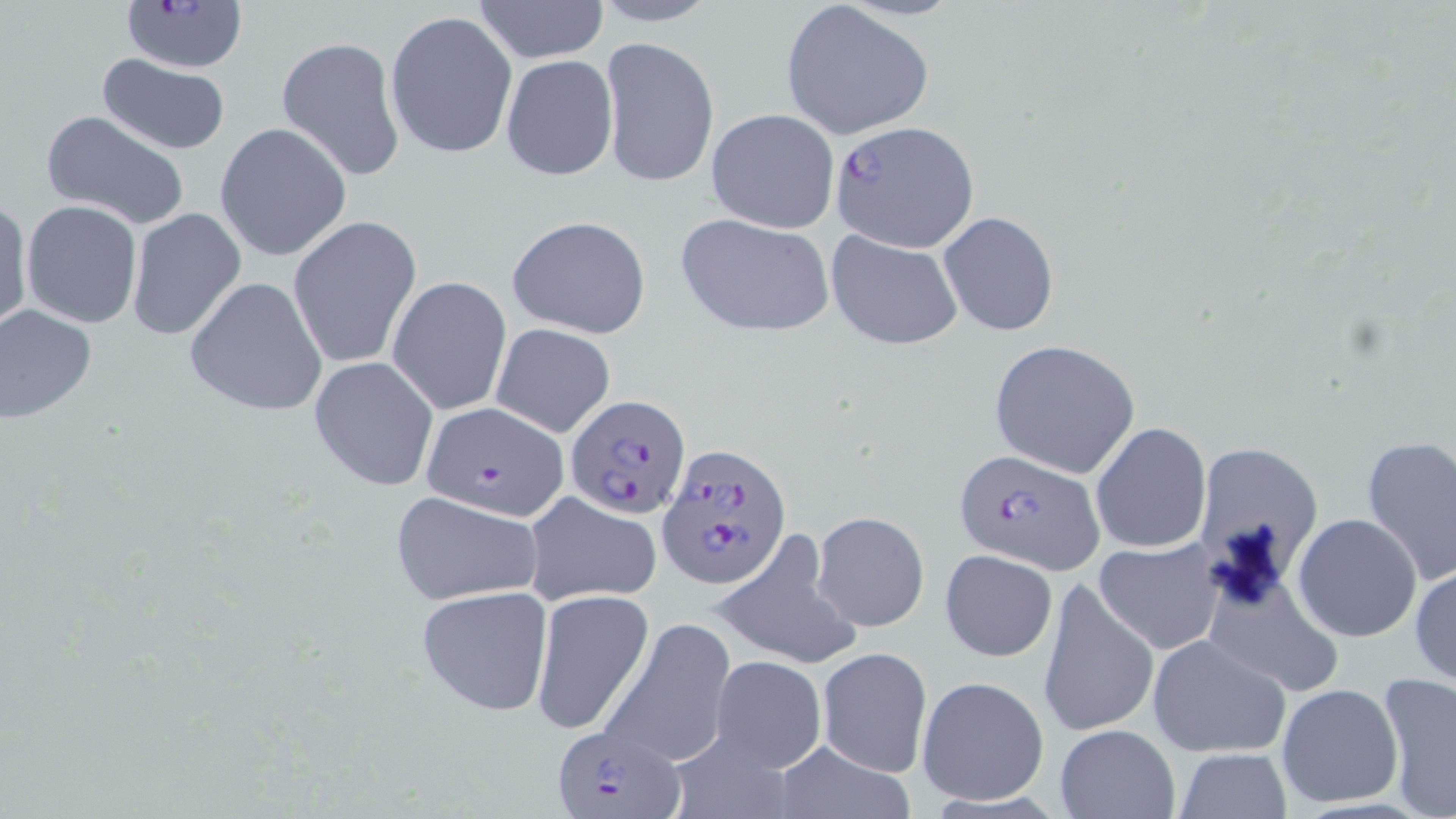

Summary:
  - Coordinate format: approximate bounding boxes as named x1/y1/x2/y2 corners in pixels
  - Plasmodium falciparum-infected red blood cell locations: (x1=121, y1=2, x2=249, y2=73), (x1=828, y1=119, x2=980, y2=251), (x1=566, y1=394, x2=691, y2=518), (x1=419, y1=401, x2=568, y2=521), (x1=658, y1=440, x2=793, y2=590), (x1=954, y1=450, x2=1102, y2=574), (x1=551, y1=720, x2=686, y2=818)
  - Uninfected red blood cell locations: (x1=587, y1=0, x2=722, y2=27), (x1=470, y1=1, x2=609, y2=65), (x1=781, y1=1, x2=933, y2=142), (x1=385, y1=10, x2=518, y2=160), (x1=600, y1=35, x2=719, y2=190), (x1=276, y1=36, x2=405, y2=181), (x1=98, y1=54, x2=230, y2=156), (x1=500, y1=55, x2=617, y2=180), (x1=40, y1=109, x2=190, y2=232), (x1=705, y1=109, x2=839, y2=232), (x1=214, y1=122, x2=351, y2=263), (x1=0, y1=198, x2=32, y2=335), (x1=21, y1=200, x2=143, y2=329), (x1=126, y1=208, x2=247, y2=342), (x1=939, y1=211, x2=1059, y2=337), (x1=675, y1=212, x2=834, y2=339), (x1=288, y1=215, x2=421, y2=369), (x1=506, y1=215, x2=652, y2=339), (x1=825, y1=231, x2=964, y2=350), (x1=387, y1=275, x2=511, y2=415), (x1=184, y1=276, x2=329, y2=418), (x1=0, y1=304, x2=98, y2=424), (x1=490, y1=322, x2=616, y2=437), (x1=987, y1=339, x2=1141, y2=479), (x1=308, y1=357, x2=438, y2=490), (x1=1091, y1=422, x2=1211, y2=554), (x1=1358, y1=435, x2=1456, y2=587), (x1=1200, y1=442, x2=1323, y2=575), (x1=387, y1=489, x2=547, y2=605), (x1=521, y1=489, x2=663, y2=606), (x1=812, y1=510, x2=928, y2=631), (x1=1293, y1=514, x2=1422, y2=643), (x1=707, y1=533, x2=864, y2=670), (x1=1094, y1=539, x2=1223, y2=655), (x1=940, y1=548, x2=1058, y2=662), (x1=1411, y1=561, x2=1455, y2=692), (x1=1038, y1=576, x2=1159, y2=740), (x1=1212, y1=579, x2=1349, y2=694), (x1=415, y1=586, x2=554, y2=716), (x1=529, y1=589, x2=653, y2=735), (x1=599, y1=616, x2=736, y2=771), (x1=1146, y1=634, x2=1290, y2=759), (x1=816, y1=647, x2=932, y2=777), (x1=710, y1=656, x2=827, y2=772), (x1=1377, y1=672, x2=1456, y2=819), (x1=916, y1=676, x2=1048, y2=805), (x1=1276, y1=682, x2=1405, y2=808), (x1=1054, y1=725, x2=1179, y2=818), (x1=772, y1=741, x2=911, y2=818), (x1=1173, y1=748, x2=1292, y2=818)
  - Slide-level diagnosis: Plasmodium falciparum
  - Modality: optical microscopy
  - Magnification: 1000x
  - Stain: May-Grünwald-Giemsa
  - Field of view: one of a larger specimen
  - Image size: 1456×819 pixels
  - Preparation: thin blood smear